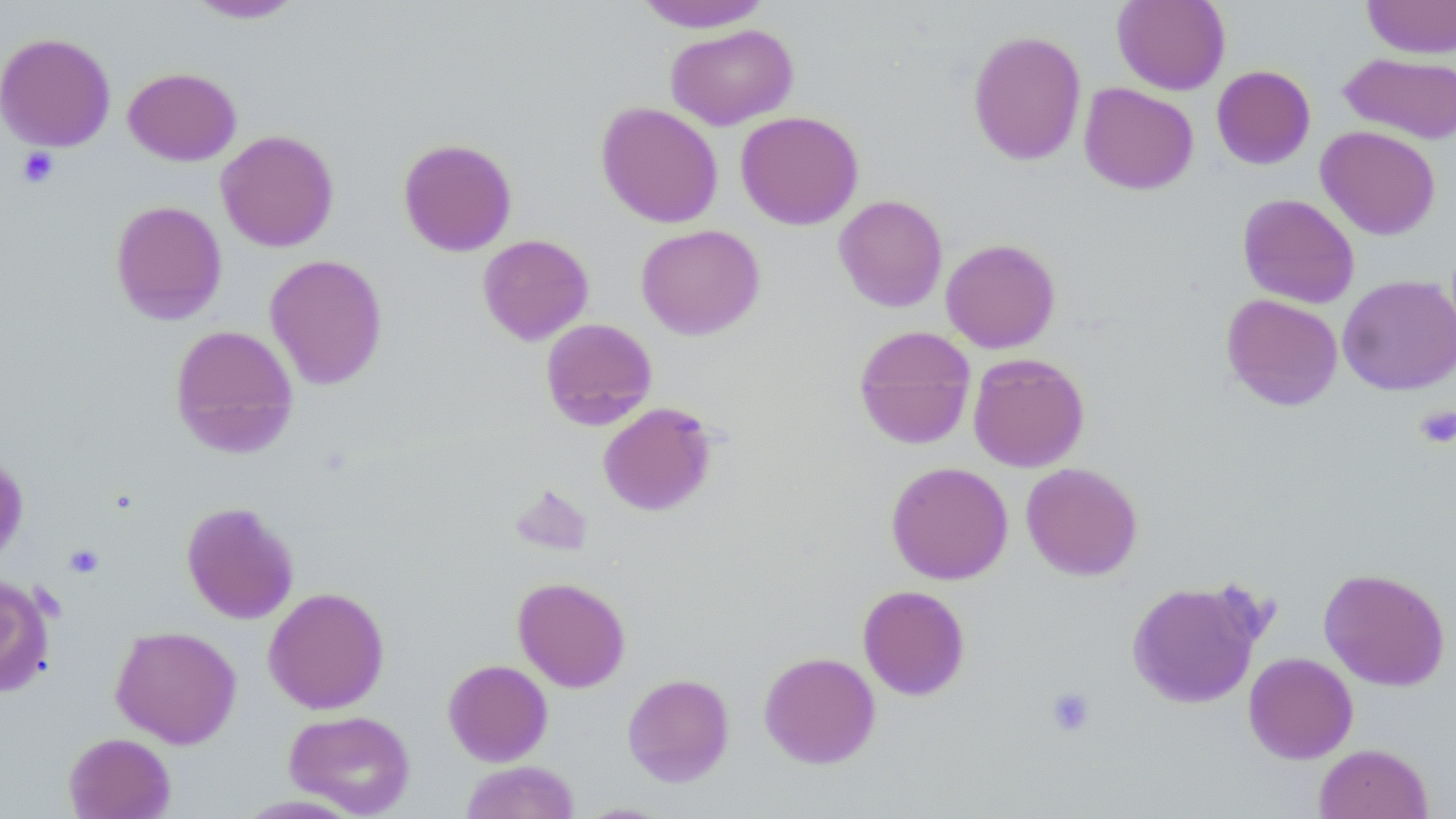

Approximate bounding boxes as (x1, y1, x2, y2) in pixels. Platelet locations: (17, 148, 59, 188), (1414, 404, 1456, 449), (64, 544, 105, 578), (1046, 686, 1096, 737). Uninfected red blood cell locations: (1111, 0, 1231, 95), (1360, 0, 1456, 59), (185, 1, 305, 23), (632, 1, 774, 33), (665, 23, 798, 130), (967, 29, 1087, 166), (0, 32, 116, 152), (1339, 52, 1456, 144), (1211, 65, 1316, 169), (123, 67, 241, 166), (1079, 83, 1199, 195), (595, 102, 723, 228), (735, 110, 863, 230), (1316, 125, 1441, 240), (216, 130, 339, 252), (398, 138, 518, 257), (1237, 193, 1360, 308), (833, 194, 948, 313), (110, 200, 228, 325), (635, 224, 765, 340), (477, 234, 594, 345), (940, 238, 1061, 353), (265, 254, 388, 390), (1337, 274, 1456, 395), (1221, 293, 1343, 411), (540, 318, 657, 431), (169, 324, 299, 457), (853, 325, 976, 449), (967, 352, 1090, 472), (597, 402, 718, 517), (0, 453, 30, 565), (886, 461, 1013, 584), (1021, 462, 1143, 580), (510, 485, 593, 556), (181, 501, 300, 624), (1318, 567, 1450, 691), (0, 574, 55, 697), (513, 576, 630, 692), (1126, 579, 1265, 709), (857, 585, 970, 700), (263, 587, 389, 714), (110, 625, 242, 749), (758, 651, 881, 769), (1243, 652, 1358, 764), (442, 659, 553, 766), (622, 673, 735, 787), (283, 709, 416, 817), (63, 732, 176, 819), (1313, 744, 1433, 819), (459, 760, 581, 819). Slide-level diagnosis: no evidence of blood parasites. 1000x magnification. Image is 1456×819 pixels. May-Grünwald-Giemsa-stained preparation. Thin blood film. One field of a larger specimen. Light microscopy.